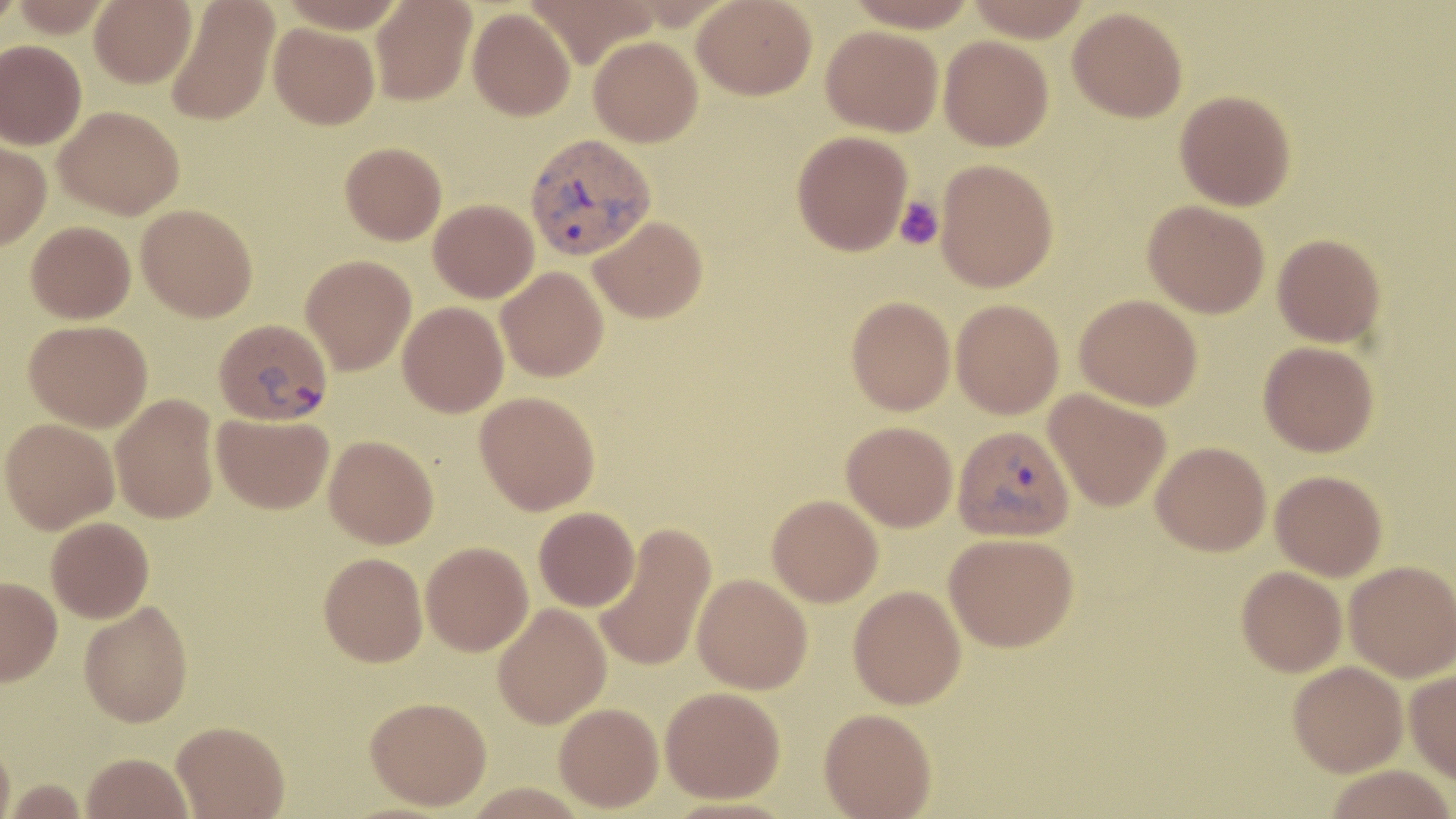
Summary:
  - Coordinate format: approximate bounding boxes as (x1, y1, x2, y2) in pixels
  - Plasmodium vivax-infected red blood cell locations: (525, 133, 655, 261), (214, 318, 333, 425), (953, 425, 1074, 542)
  - Uninfected red blood cell locations: (0, 0, 25, 33), (9, 0, 115, 37), (89, 0, 196, 88), (279, 0, 406, 33), (371, 0, 476, 105), (526, 0, 661, 68), (693, 0, 817, 100), (843, 0, 978, 32), (966, 0, 1093, 42), (166, 1, 279, 126), (1067, 6, 1188, 122), (467, 7, 575, 120), (269, 23, 379, 129), (821, 25, 943, 136), (588, 36, 703, 147), (939, 36, 1053, 151), (0, 40, 86, 150), (1175, 89, 1297, 210), (55, 105, 184, 219), (792, 131, 913, 256), (0, 140, 51, 249), (340, 142, 447, 245), (935, 159, 1059, 291), (428, 199, 538, 302), (1143, 200, 1270, 319), (136, 204, 258, 322), (590, 216, 708, 323), (25, 221, 136, 323), (1273, 233, 1386, 347), (300, 254, 416, 375), (496, 267, 609, 382), (1075, 294, 1202, 410), (846, 296, 955, 415), (951, 298, 1064, 419), (398, 302, 508, 417), (23, 320, 152, 432), (1258, 341, 1378, 456), (1045, 390, 1171, 512), (474, 391, 600, 515), (110, 394, 219, 523), (212, 413, 334, 514), (1, 418, 119, 533), (841, 421, 958, 531), (324, 434, 438, 548), (1151, 441, 1271, 556), (1270, 470, 1388, 581), (767, 495, 883, 607), (534, 507, 640, 611), (46, 517, 154, 623), (594, 523, 716, 673), (944, 532, 1078, 652), (420, 542, 533, 656), (318, 552, 428, 666), (1344, 560, 1456, 682), (1237, 566, 1347, 676), (693, 573, 813, 694), (0, 577, 61, 686), (848, 585, 966, 709), (79, 601, 193, 727), (493, 603, 611, 729), (1288, 660, 1408, 776), (1405, 670, 1456, 783), (660, 686, 785, 802), (364, 696, 492, 810), (554, 702, 663, 812), (819, 707, 936, 818), (172, 720, 289, 818), (0, 738, 15, 819), (82, 752, 193, 819), (1323, 764, 1456, 819), (4, 779, 90, 818)
  - Platelet locations: (894, 196, 943, 250)
  - Slide-level diagnosis: Plasmodium vivax
  - Preparation: thin blood smear
  - Magnification: 1000x
  - Stain: May-Grünwald-Giemsa
  - Modality: light microscopy
  - Field of view: single
  - Image size: 1456×819 pixels